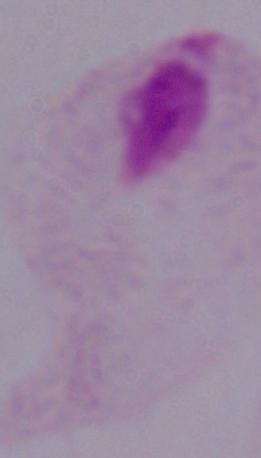

modality: micrograph
magnification: 1000x
identification: trichomonad